Assess this cell for malaria.
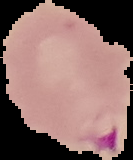

Parasitized.

The area outside the segmented cell region is set to black. Image is 133×160 pixels. From a thin blood film.